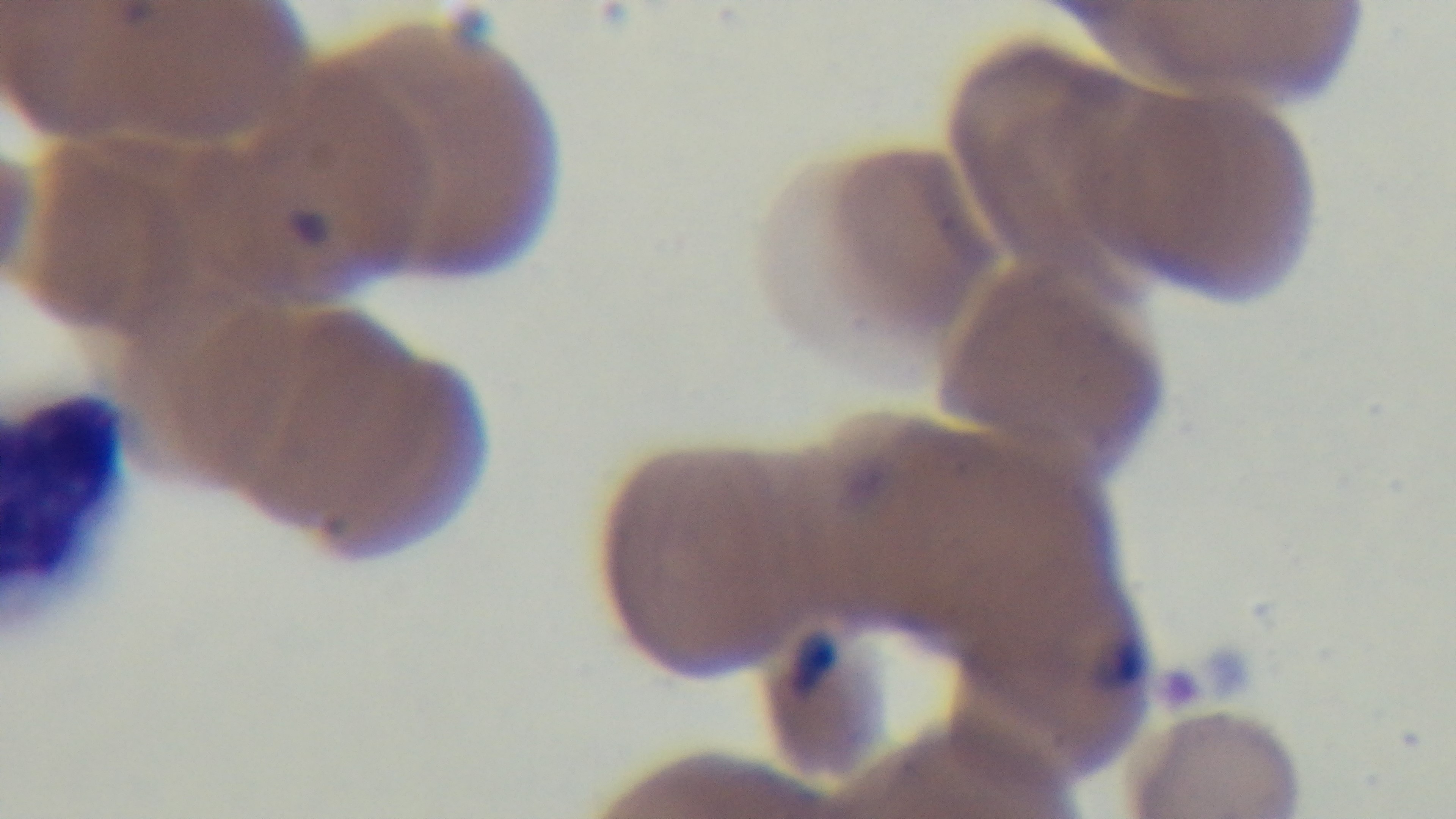

objective: 100x oil immersion
field_of_view: single
stain: Giemsa
preparation: thin smear
capture: mounted 4K digital camera
malaria_status: infected
modality: light microscopy